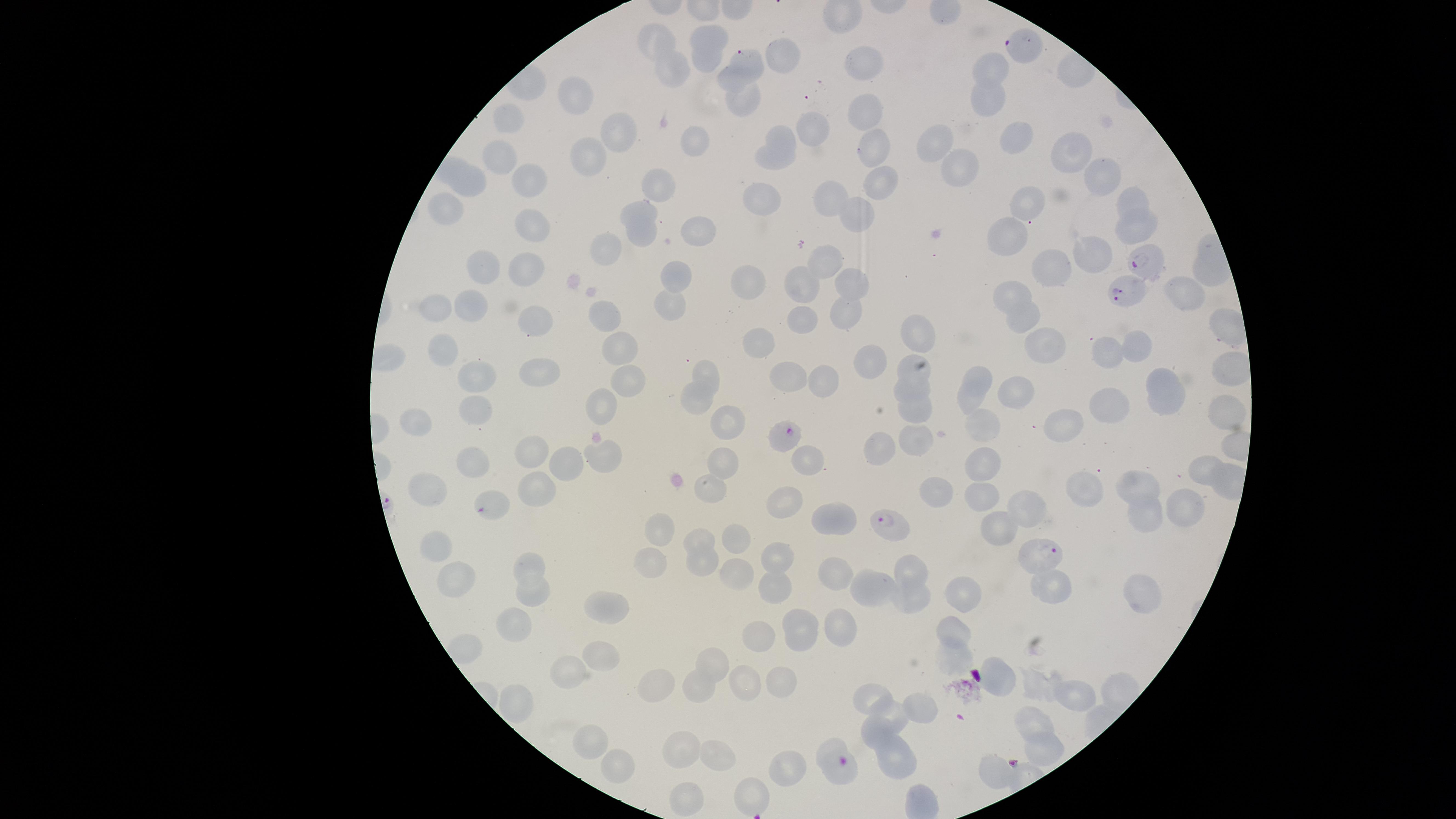
capture = smartphone photograph through the microscope eyepiece
presence = malaria parasites identified
uninfected red blood cells = approximate marker points as {x, y} in pixels: {715, 31}, {654, 42}, {706, 60}, {788, 62}, {864, 62}, {994, 67}, {667, 72}, {732, 80}, {989, 97}, {578, 100}, {745, 103}, {862, 106}, {516, 123}, {808, 128}, {622, 134}, {783, 135}, {933, 136}, {1014, 136}, {696, 138}, {876, 147}, {1066, 148}, {508, 161}, {770, 161}, {583, 162}, {1102, 169}, {963, 174}, {475, 176}, {530, 178}, {879, 181}, {661, 184}, {830, 193}, {765, 198}, {1027, 201}, {1129, 202}, {447, 210}, {634, 212}, {857, 213}, {532, 220}, {1135, 229}, {696, 233}, {638, 234}, {1010, 234}, {615, 248}, {1093, 252}, {822, 258}, {481, 268}, {523, 268}, {1054, 272}, {681, 275}, {746, 279}, {851, 281}, {797, 282}, {1015, 290}, {1184, 293}, {676, 298}, {470, 301}, {439, 305}, {846, 308}, {603, 317}, {1023, 317}, {805, 320}, {534, 325}, {912, 330}, {1141, 338}, {760, 340}, {433, 346}, {623, 347}, {1044, 347}, {1111, 349}, {872, 357}, {909, 366}, {706, 371}, {478, 376}, {798, 377}, {632, 378}, {536, 379}, {976, 379}, {826, 381}, {914, 389}, {1022, 394}, {697, 399}, {1173, 400}, {599, 401}, {970, 401}, {471, 405}, {1113, 407}, {921, 409}, {1221, 411}, {409, 415}, {726, 421}, {1062, 422}, {983, 423}, {913, 437}, {886, 453}, {531, 455}, {600, 458}, {721, 459}, {806, 460}, {470, 463}, {569, 463}, {981, 465}, {1200, 467}, {1146, 482}, {713, 484}, {535, 488}, {1100, 489}, {427, 491}, {942, 491}, {976, 493}, {784, 503}, {1030, 507}, {1183, 508}, {1140, 515}, {832, 517}, {1001, 527}, {664, 532}, {703, 535}, {737, 539}, {438, 552}, {700, 561}, {777, 561}, {533, 565}, {650, 569}, {910, 569}, {838, 573}, {456, 577}, {733, 583}, {1055, 589}, {772, 591}, {868, 591}, {1137, 592}, {963, 594}, {905, 595}, {536, 597}, {612, 607}, {952, 624}, {843, 625}, {802, 628}, {518, 629}, {760, 637}, {601, 655}, {953, 656}, {714, 663}, {577, 670}, {1004, 676}, {780, 680}, {658, 683}, {745, 683}, {699, 685}, {1040, 686}, {1080, 695}, {868, 697}, {519, 705}, {920, 710}, {888, 718}, {1036, 723}, {593, 741}, {831, 743}, {1043, 746}, {684, 753}, {892, 756}, {721, 761}, {615, 766}, {786, 766}, {990, 769}, {837, 770}, {754, 794}, {687, 796}
stain = Giemsa
field of view = single
species = Plasmodium falciparum
preparation = thin blood film
visible region = circular
image size = 1456×819 pixels
parasitized red blood cells = approximate marker points as {x, y} in pixels: {1025, 41}, {747, 58}, {1144, 263}, {1128, 293}, {789, 436}, {481, 511}, {892, 524}, {1037, 555}